Locate every blood parasite and identify its species.
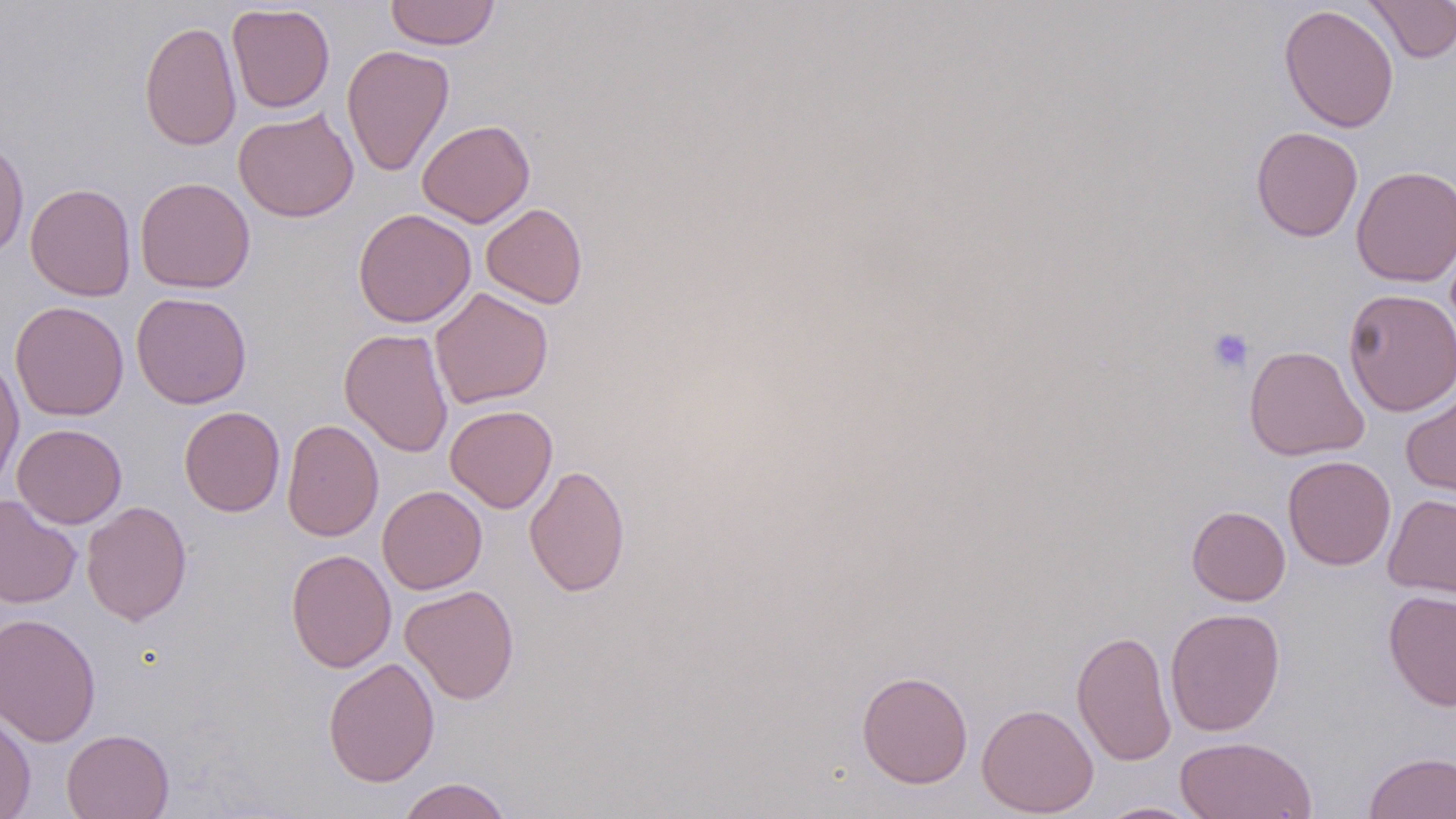
No blood parasites seen.

Approximate bounding boxes as [x1, y1, x2, y2] in pixels. Platelet locations: [1206, 328, 1254, 375]. Uninfected red blood cell locations: [384, 0, 501, 50], [1363, 0, 1456, 63], [226, 3, 335, 113], [1278, 4, 1399, 133], [139, 20, 241, 151], [342, 44, 454, 177], [233, 108, 359, 222], [417, 119, 535, 227], [1250, 126, 1363, 242], [0, 136, 29, 258], [1351, 166, 1456, 286], [135, 176, 255, 294], [25, 183, 136, 301], [481, 203, 587, 308], [352, 208, 476, 327], [429, 287, 553, 408], [1342, 288, 1456, 417], [131, 291, 252, 409], [10, 301, 129, 421], [339, 328, 454, 457], [1243, 345, 1369, 461], [0, 355, 25, 492], [1400, 386, 1456, 500], [445, 405, 558, 513], [179, 406, 285, 517], [281, 419, 384, 542], [12, 423, 127, 528], [1283, 455, 1396, 570], [524, 464, 630, 597], [377, 485, 487, 594], [1383, 493, 1456, 598], [0, 494, 82, 608], [81, 501, 192, 625], [1187, 505, 1290, 605], [285, 549, 396, 673], [400, 585, 520, 705], [1384, 589, 1456, 711], [1165, 608, 1285, 736], [0, 612, 101, 747], [1071, 628, 1176, 767], [323, 657, 440, 787], [856, 670, 974, 788], [976, 702, 1098, 817], [0, 707, 36, 819], [61, 728, 174, 819], [1174, 735, 1317, 819], [1363, 751, 1456, 818], [397, 777, 513, 819], [1095, 801, 1208, 818]. Slide-level diagnosis: negative for blood parasites. Single field of view. Light microscopy. Thin blood film. Image is 1456×819 pixels. May-Grünwald-Giemsa stain. 1000x magnification.